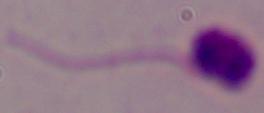
Summary:
  - Modality: micrograph
  - Magnification: 1000x
  - Identification: Leishmania